State the preparation type.
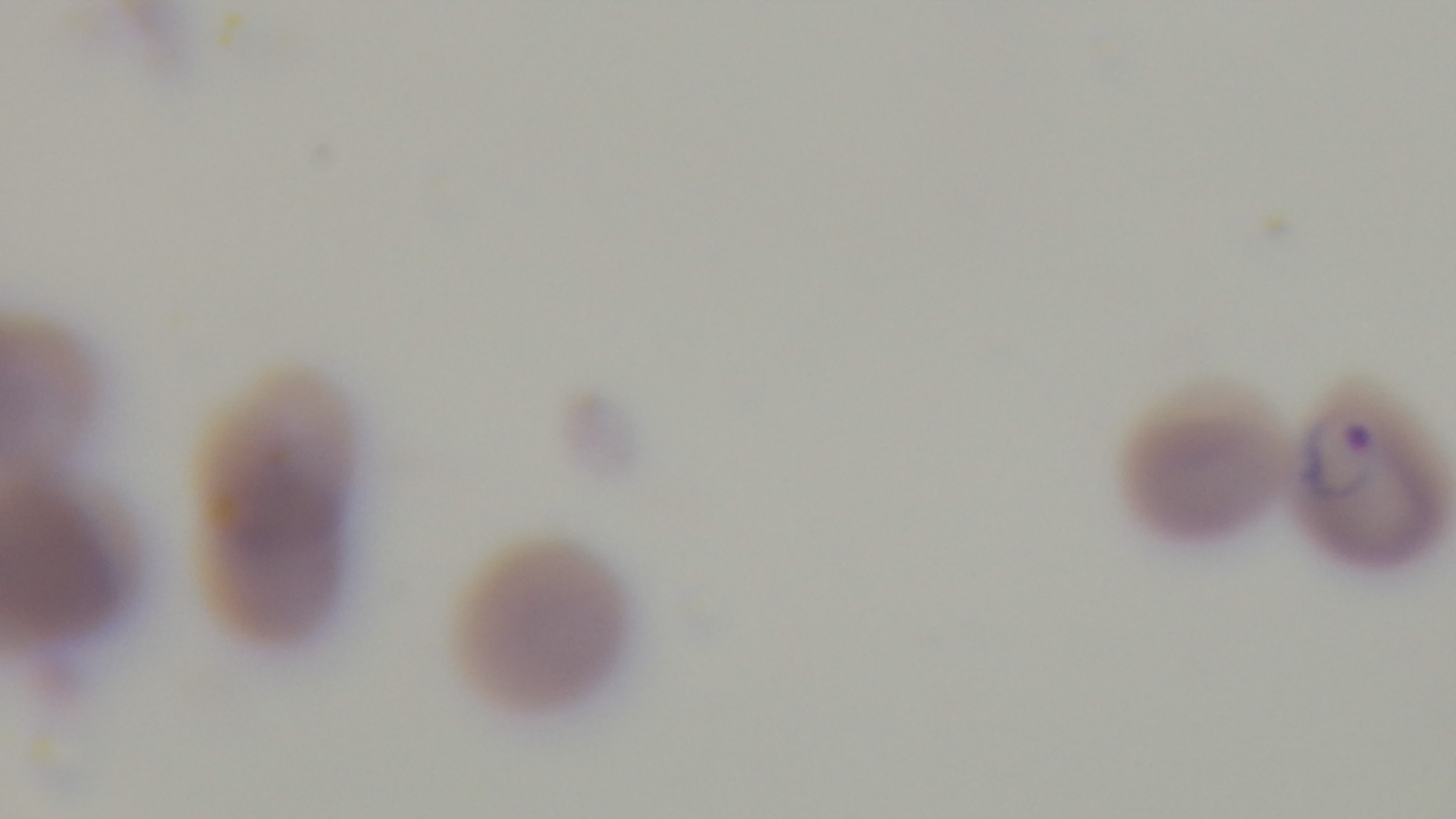

Thin.

Captured with a mounted 4K digital camera. Malaria status: positive. Giemsa stain. Oil-immersion objective, 100x. Single field of view. Photomicrograph.